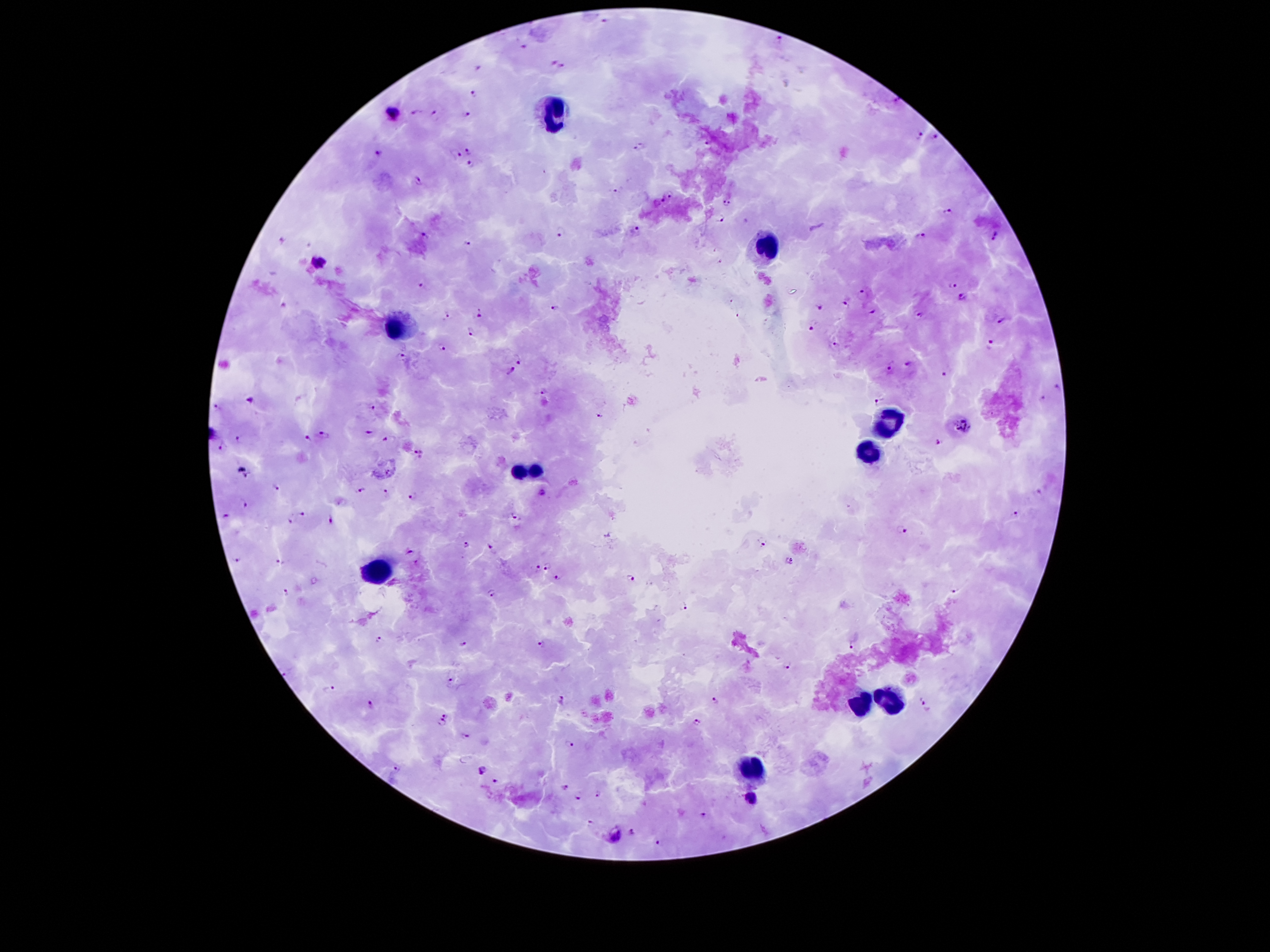

{
  "patient_malaria_status": "positive for Plasmodium falciparum",
  "image_size": "1270×952 pixels",
  "leukocyte_locations": "approximate centers as (x, y) in pixels: (554, 108), (767, 249), (394, 325), (885, 422), (868, 454), (525, 473), (379, 575), (858, 701), (890, 701), (747, 767)",
  "capture": "smartphone through the microscope eyepiece",
  "preparation": "thick blood film",
  "magnification": "100x",
  "malaria_parasite_locations": "approximate centers as (x, y) in pixels: (606, 20), (780, 40), (524, 46), (551, 63), (564, 66), (478, 68), (474, 93), (416, 110), (393, 111), (466, 113), (434, 114), (921, 135), (935, 136), (470, 149), (639, 149), (380, 151), (457, 154), (472, 164), (420, 181), (614, 190), (673, 193), (662, 199), (727, 201), (949, 211), (719, 217), (635, 227), (562, 229), (425, 233), (922, 236), (997, 236), (283, 239), (469, 241), (318, 263), (422, 283), (951, 286), (863, 293), (962, 297), (731, 300), (818, 306), (844, 306), (556, 308), (481, 311), (873, 312), (921, 314), (448, 315), (739, 318), (1000, 322), (812, 326), (470, 330), (989, 342), (833, 344), (441, 348), (518, 357), (402, 358), (910, 364), (894, 365), (512, 368), (947, 372), (1059, 388), (544, 390), (251, 399), (1041, 399), (878, 401), (216, 406), (371, 406), (600, 416), (963, 425), (369, 432), (325, 433), (386, 438), (238, 439), (308, 439), (939, 442), (221, 444), (420, 452), (248, 474), (276, 488), (360, 490), (1042, 490), (386, 492), (543, 494), (413, 496), (243, 503), (300, 512), (1016, 513), (516, 515), (225, 517), (330, 520), (290, 521), (904, 530), (761, 540), (466, 543), (490, 546), (408, 552), (235, 559), (281, 561), (788, 561), (546, 564), (538, 566), (558, 577), (630, 577), (489, 590), (956, 590), (286, 593), (683, 604), (379, 638), (463, 642), (542, 643), (853, 645), (789, 664), (450, 678), (326, 689), (713, 700), (562, 702), (372, 703), (925, 706), (446, 715), (440, 722), (698, 722), (465, 735), (568, 744), (399, 768), (482, 768), (495, 781), (566, 785), (598, 792), (578, 797), (751, 797), (705, 816), (591, 820), (633, 832), (616, 839), (658, 842)",
  "stain": "Giemsa",
  "field_of_view": "single"
}